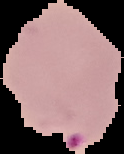
Summary:
  - Image size: 124×154 pixels
  - Result: Plasmodium parasites detected
  - Preparation: thin blood smear
  - Image type: segmented cell region with the area outside set to black